Describe the morphology of the red blood cells.
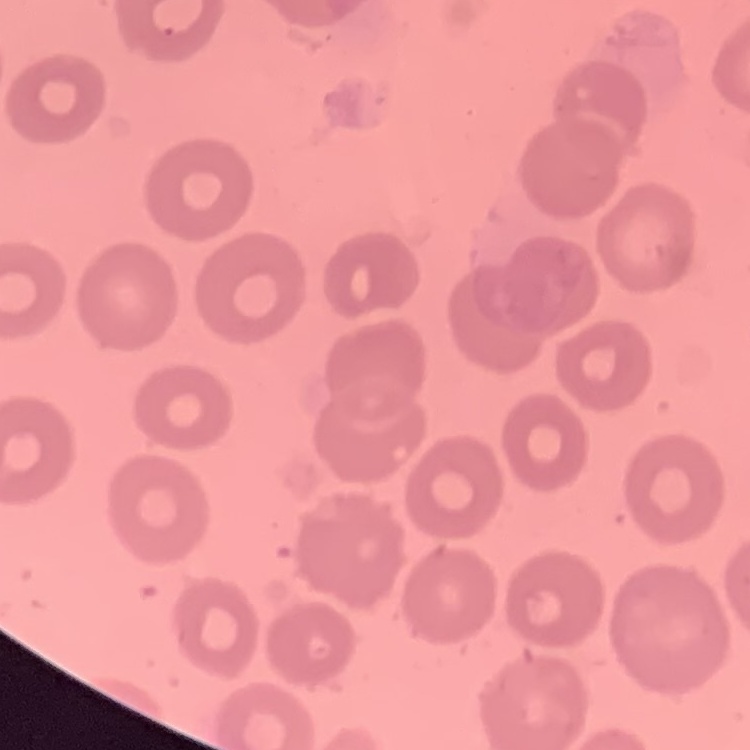
No rouleaux formation.

Summary:
  - Stain: Field's or Giemsa
  - Preparation: thin blood smear
  - Image type: square crop of a larger photomicrograph